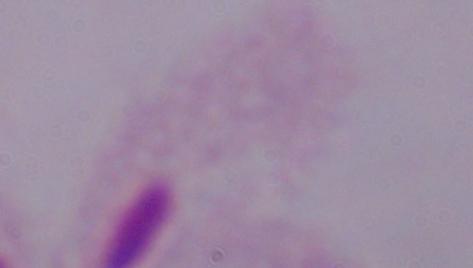

{
  "modality": "photomicrograph",
  "identification": "trichomonad",
  "magnification": "1000x"
}